Name the parasite shown.
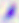
Toxoplasma gondii.

Micrograph. Captured at 400x magnification.